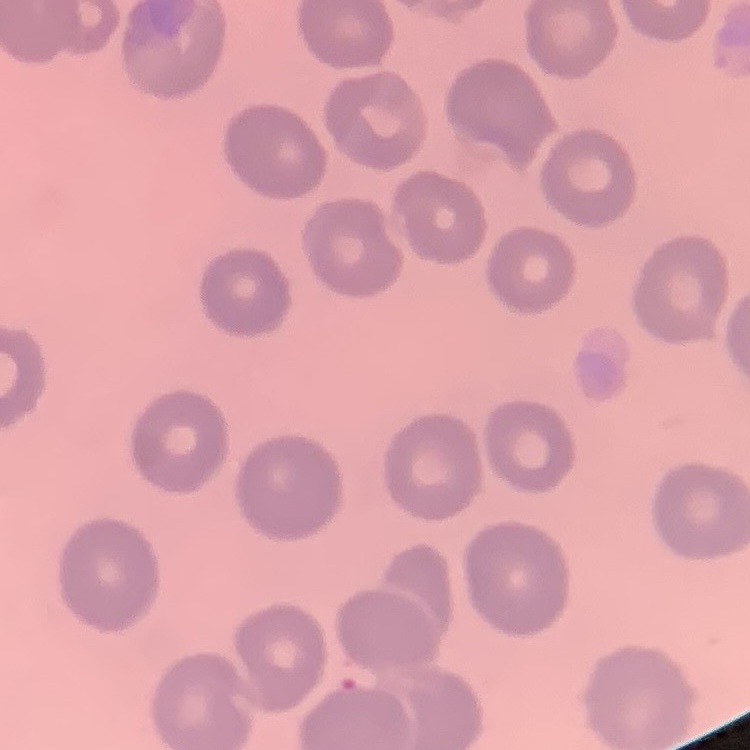 The erythrocytes show no rouleaux formation. One tile cut from a larger photomicrograph. Thin blood film. Field's or Giemsa stain.